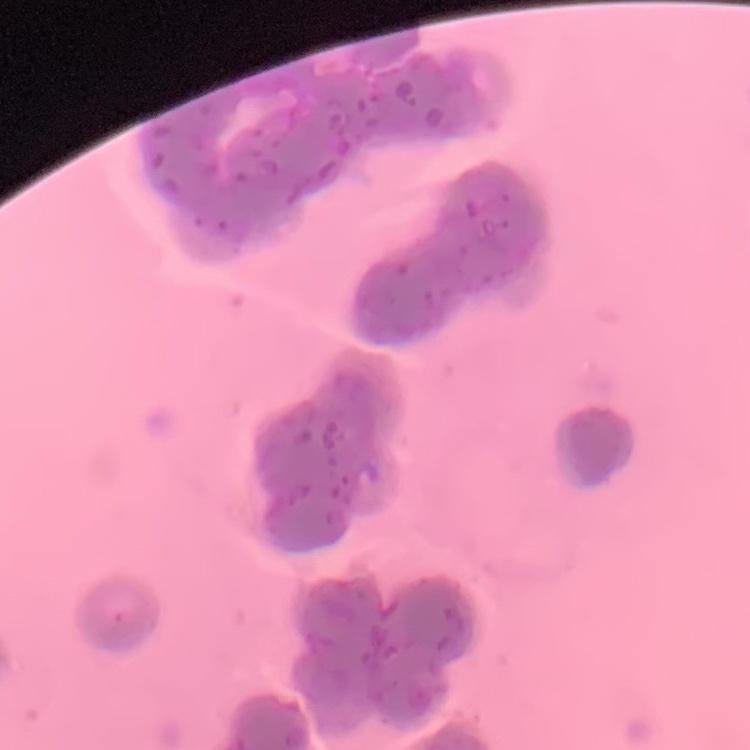
red blood cell morphology = rouleaux formation
image type = square crop of a larger photomicrograph
preparation = thin blood film
stain = Field's or Giemsa